Assess the morphology of the erythrocytes.
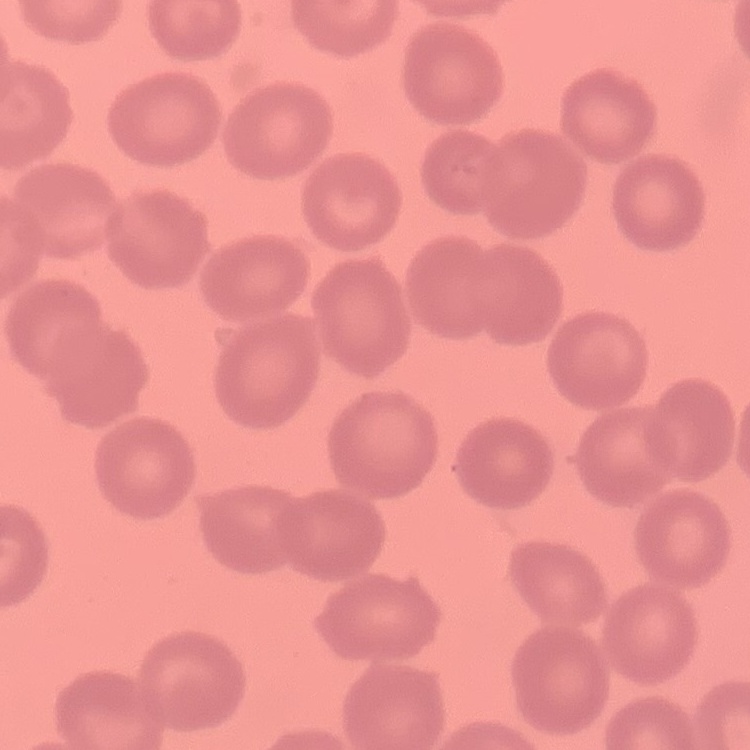
They show no rouleaux formation.

image type = one tile cut from a larger photomicrograph
preparation = thin blood film
stain = Field's or Giemsa